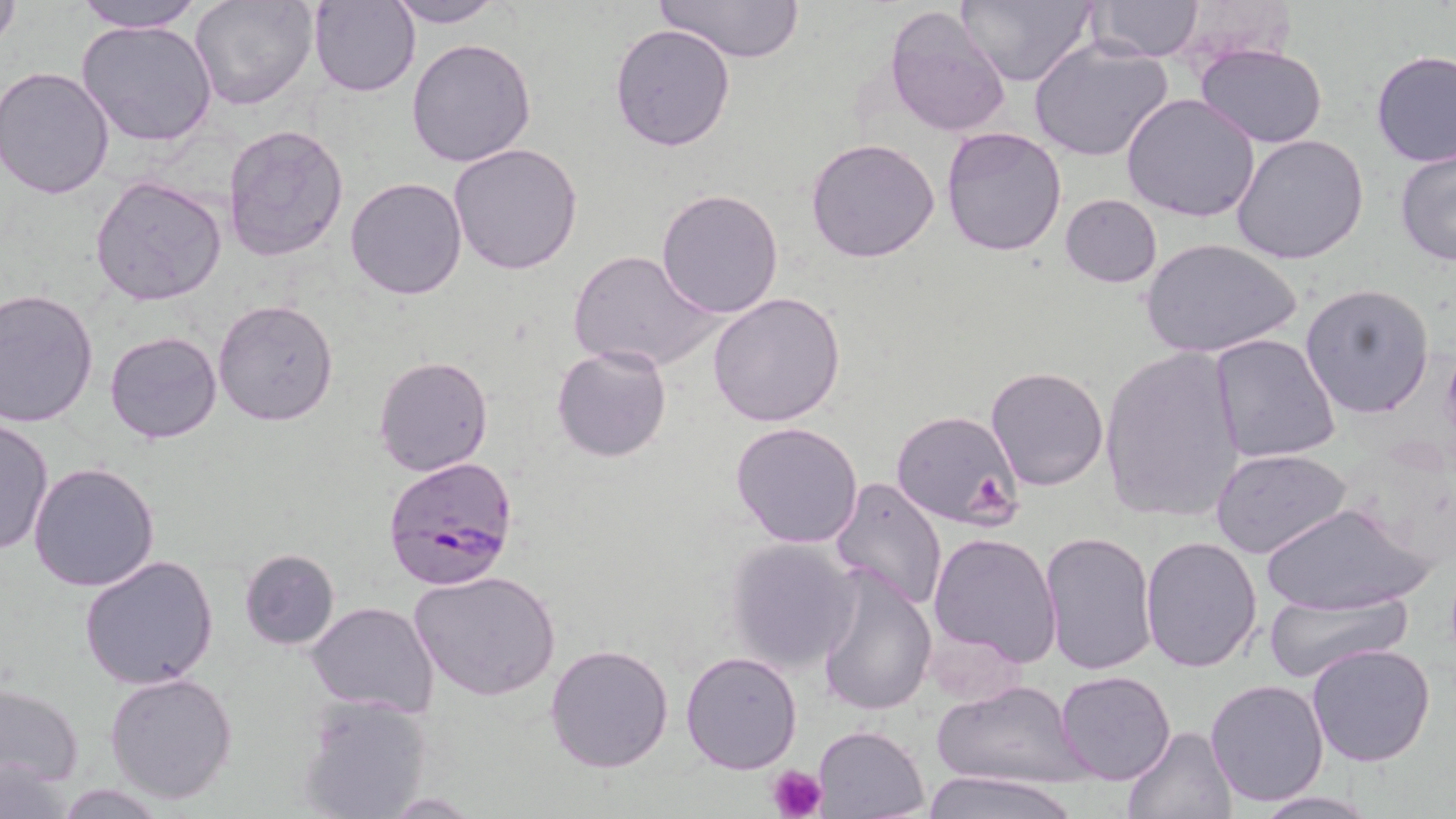

Summary:
  - Coordinate format: approximate bounding boxes as (x1,y1)-(x2,y2) corner pairs in pixels
  - Plasmodium falciparum-infected red blood cell locations: (382,455)-(519,593)
  - Platelet locations: (968,476)-(1016,525), (766,762)-(828,819)
  - Uninfected red blood cell locations: (74,0)-(207,33), (190,0)-(317,112), (308,0)-(418,96), (655,0)-(805,64), (958,0)-(1100,89), (1088,0)-(1203,60), (384,1)-(506,28), (883,2)-(1014,138), (0,3)-(23,51), (76,19)-(216,148), (610,22)-(737,152), (406,36)-(537,169), (1030,40)-(1173,160), (1196,43)-(1329,147), (1371,49)-(1455,167), (2,66)-(118,199), (1121,94)-(1261,224), (221,124)-(349,264), (940,126)-(1067,256), (1230,132)-(1371,265), (805,137)-(940,263), (449,141)-(584,275), (1394,146)-(1455,267), (90,174)-(227,305), (344,176)-(468,300), (656,188)-(785,319), (1060,193)-(1163,287), (1139,238)-(1302,358), (567,250)-(719,373), (1301,282)-(1436,418), (1,289)-(100,428), (707,293)-(847,428), (214,298)-(340,427), (105,330)-(222,444), (1208,335)-(1342,464), (550,345)-(672,462), (1099,345)-(1246,522), (373,354)-(494,477), (985,365)-(1110,490), (889,413)-(1023,531), (0,418)-(53,558), (730,421)-(864,549), (1211,448)-(1353,562), (29,460)-(161,593), (829,476)-(947,612), (1260,501)-(1431,618), (1039,530)-(1157,675), (927,531)-(1063,668), (1139,533)-(1264,672), (722,538)-(863,673), (237,547)-(340,651), (78,553)-(221,690), (813,562)-(937,720), (411,569)-(559,703), (1263,589)-(1410,681), (306,602)-(440,716), (545,642)-(677,774), (1306,643)-(1437,767), (680,650)-(802,774), (1054,671)-(1178,785), (105,673)-(238,805), (935,679)-(1083,788), (1205,679)-(1330,807), (0,683)-(83,788), (295,695)-(434,818), (1121,723)-(1236,818), (812,725)-(929,818), (0,756)-(70,819), (923,769)-(1079,819), (51,783)-(167,817), (1248,791)-(1379,817), (382,793)-(482,816)
  - Slide-level diagnosis: Plasmodium falciparum
  - Preparation: thin blood smear
  - Magnification: 1000x
  - Field of view: one of a larger specimen
  - Image size: 1456×819 pixels
  - Stain: May-Grünwald-Giemsa
  - Modality: optical microscopy